Outline every parasitised red blood cell, every trophozoite, every gametocyte, every leukocyte, and every artifact (platelet-like body, stain precipitate, or debris).
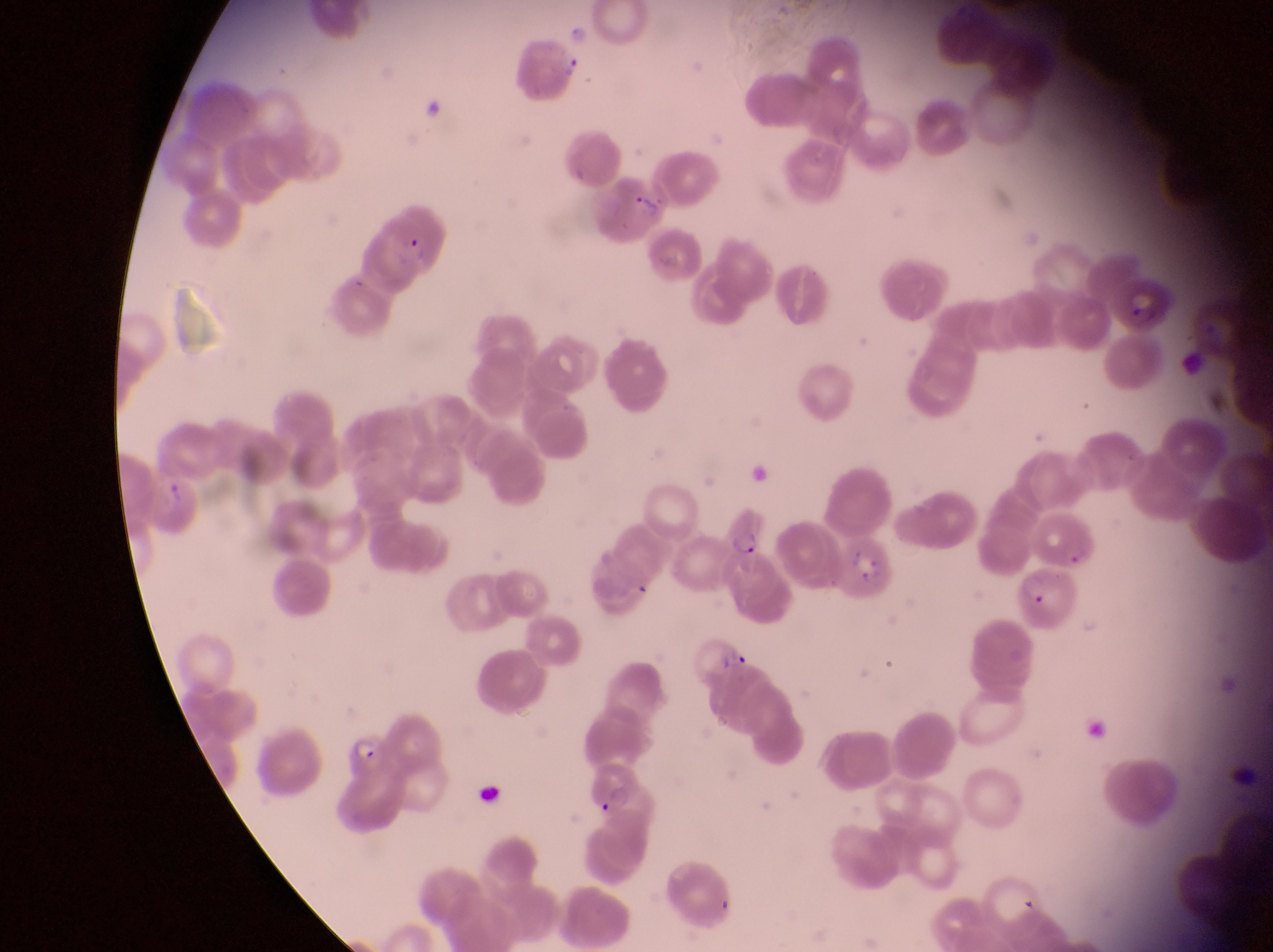

Approximate bounding boxes as (left, top, right, bottom) in pixels.
Parasitised red blood cells: (514, 42, 595, 109), (595, 174, 669, 239), (371, 201, 450, 286), (1117, 272, 1175, 333), (726, 502, 773, 559), (841, 535, 903, 602), (1018, 561, 1078, 633), (347, 724, 394, 777).
No leukocytes observed.

Summary:
  - Preparation: thin blood film
  - Magnification: 1000x
  - Capture: smartphone photograph through the eyepiece of an Olympus CX-23 microscope
  - Image size: 1273×952 pixels
  - Country: Uganda
  - Field of view: single